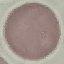

result = no malaria parasites seen
image type = automatically extracted cell patch, resized to 64 × 64 pixels
capture = smartphone camera at the microscope eyepiece
stain = Giemsa
preparation = thin blood film